Name the blood parasite species.
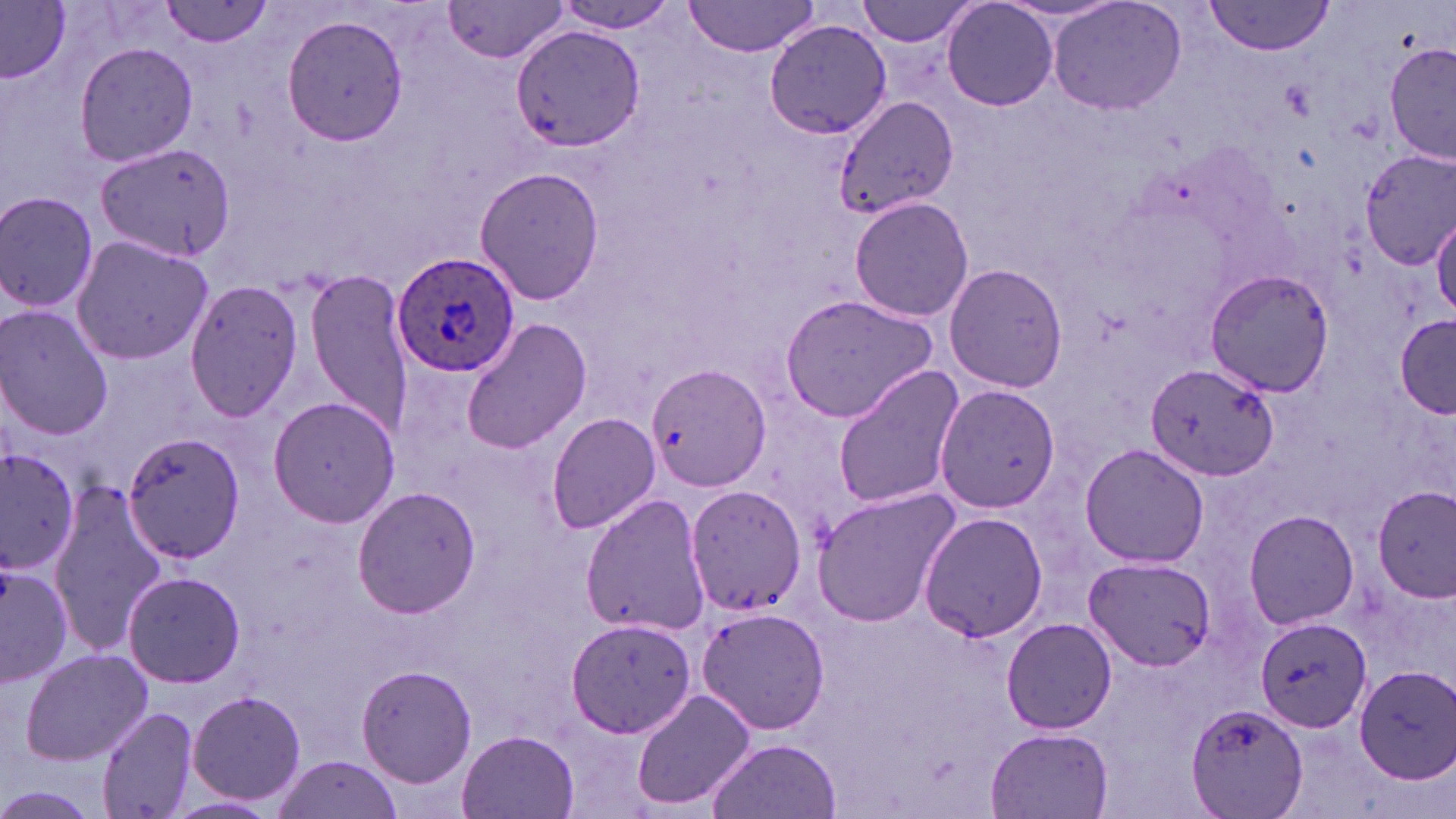

Plasmodium ovale.

stain = May-Grünwald-Giemsa
Plasmodium ovale-infected red blood cell locations = approximate bounding boxes as named x1/y1/x2/y2 corners in pixels: (x1=391, y1=249, x2=519, y2=379)
uninfected red blood cell locations = approximate bounding boxes as named x1/y1/x2/y2 corners in pixels: (x1=160, y1=0, x2=275, y2=47), (x1=684, y1=0, x2=822, y2=57), (x1=856, y1=0, x2=982, y2=48), (x1=940, y1=0, x2=1059, y2=112), (x1=0, y1=1, x2=71, y2=83), (x1=1046, y1=1, x2=1188, y2=117), (x1=1202, y1=2, x2=1336, y2=55), (x1=441, y1=3, x2=573, y2=63), (x1=550, y1=3, x2=684, y2=34), (x1=280, y1=15, x2=409, y2=146), (x1=763, y1=17, x2=892, y2=139), (x1=509, y1=24, x2=642, y2=152), (x1=72, y1=41, x2=197, y2=169), (x1=1386, y1=42, x2=1454, y2=169), (x1=833, y1=94, x2=959, y2=219), (x1=94, y1=139, x2=239, y2=263), (x1=1358, y1=148, x2=1456, y2=270), (x1=475, y1=164, x2=602, y2=306), (x1=0, y1=189, x2=101, y2=315), (x1=849, y1=196, x2=975, y2=321), (x1=1430, y1=212, x2=1455, y2=318), (x1=69, y1=233, x2=218, y2=366), (x1=943, y1=261, x2=1068, y2=393), (x1=1203, y1=269, x2=1335, y2=396), (x1=305, y1=272, x2=412, y2=429), (x1=183, y1=278, x2=302, y2=423), (x1=779, y1=294, x2=943, y2=422), (x1=0, y1=306, x2=115, y2=439), (x1=1396, y1=314, x2=1456, y2=414), (x1=461, y1=316, x2=590, y2=453), (x1=1145, y1=363, x2=1276, y2=481), (x1=648, y1=364, x2=768, y2=492), (x1=831, y1=366, x2=965, y2=510), (x1=934, y1=385, x2=1062, y2=513), (x1=267, y1=394, x2=401, y2=527), (x1=545, y1=412, x2=662, y2=534), (x1=120, y1=431, x2=248, y2=562), (x1=1079, y1=444, x2=1209, y2=570), (x1=0, y1=449, x2=83, y2=575), (x1=49, y1=483, x2=166, y2=655), (x1=684, y1=483, x2=807, y2=617), (x1=351, y1=485, x2=483, y2=618), (x1=1372, y1=485, x2=1455, y2=601), (x1=810, y1=488, x2=961, y2=628), (x1=580, y1=493, x2=708, y2=637), (x1=1243, y1=508, x2=1357, y2=630), (x1=917, y1=510, x2=1050, y2=644), (x1=1084, y1=556, x2=1215, y2=672), (x1=0, y1=558, x2=74, y2=684), (x1=122, y1=571, x2=245, y2=689), (x1=695, y1=606, x2=831, y2=735), (x1=1255, y1=615, x2=1374, y2=733), (x1=1001, y1=616, x2=1118, y2=735), (x1=566, y1=617, x2=695, y2=737), (x1=20, y1=648, x2=153, y2=763), (x1=355, y1=664, x2=477, y2=788), (x1=1352, y1=664, x2=1456, y2=784), (x1=186, y1=690, x2=307, y2=808), (x1=632, y1=690, x2=753, y2=813), (x1=1186, y1=701, x2=1311, y2=819), (x1=97, y1=707, x2=200, y2=819), (x1=986, y1=726, x2=1115, y2=818), (x1=458, y1=731, x2=578, y2=817), (x1=705, y1=733, x2=842, y2=817), (x1=272, y1=754, x2=405, y2=818)
field of view = one of a larger specimen
magnification = 1000x
modality = optical microscopy
image size = 1456×819 pixels
preparation = thin blood smear